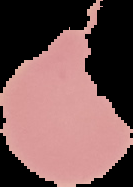

Image is 133×187 pixels. Cell region segmented out of the field of view; the surrounding area is masked to black. Malaria status: uninfected. From a thin blood smear.